Describe the morphology of the red blood cells.
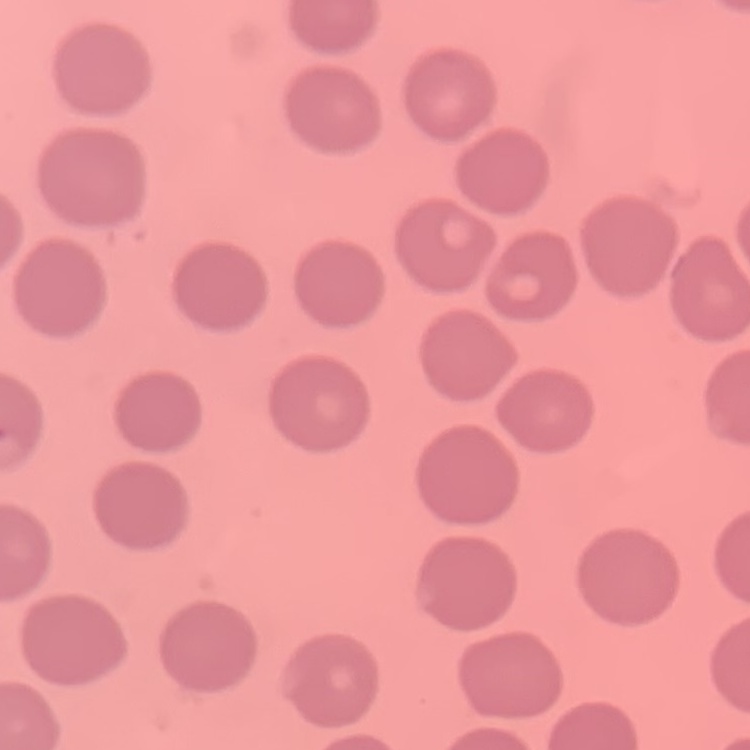

No rouleaux formation.

Field's or Giemsa stain. Thin blood smear. Square crop of a larger photomicrograph.